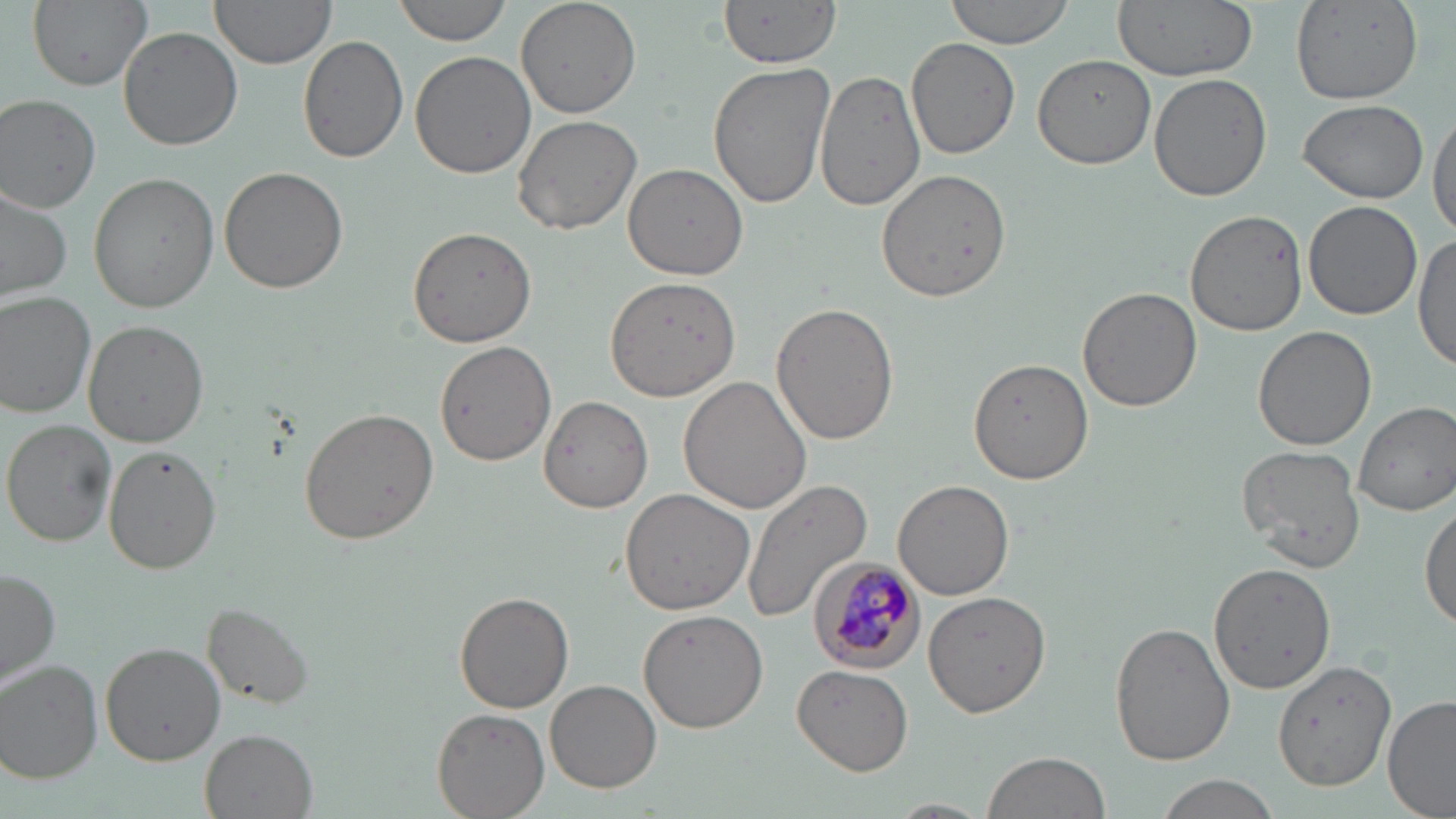

slide_level_diagnosis: Plasmodium malariae
magnification: 1000x
plasmodium_malariae_infected_red_blood_cell_locations: 'approximate bounding boxes as [x1, y1, x2, y2] in pixels: [809, 559, 924, 673]'
preparation: thin blood smear
modality: light microscopy
stain: May-Grünwald-Giemsa
image_size: 1456×819 pixels
uninfected_red_blood_cell_locations: 'approximate bounding boxes as [x1, y1, x2, y2] in pixels: [26, 0, 152, 91], [211, 0, 335, 70], [393, 0, 513, 44], [515, 0, 642, 118], [720, 0, 838, 68], [945, 0, 1079, 49], [1113, 0, 1259, 80], [1289, 1, 1423, 105], [118, 26, 243, 151], [298, 34, 409, 164], [906, 37, 1020, 159], [409, 51, 535, 180], [1032, 54, 1157, 170], [708, 61, 835, 209], [815, 66, 924, 213], [1149, 73, 1272, 204], [1, 95, 101, 212], [1299, 99, 1428, 203], [1429, 107, 1456, 235], [512, 114, 641, 235], [621, 162, 748, 279], [219, 167, 349, 295], [877, 168, 1013, 302], [91, 172, 220, 311], [0, 184, 72, 304], [1303, 201, 1422, 320], [1184, 209, 1308, 334], [406, 225, 539, 349], [1413, 232, 1456, 374], [603, 276, 739, 400], [1077, 287, 1202, 410], [0, 291, 98, 416], [771, 304, 899, 443], [84, 321, 207, 447], [1252, 324, 1377, 449], [435, 341, 558, 467], [970, 358, 1094, 484], [678, 375, 811, 514], [538, 394, 654, 513], [1354, 401, 1456, 515], [299, 408, 439, 544], [3, 419, 116, 545], [1236, 444, 1366, 573], [103, 446, 224, 574], [742, 480, 872, 622], [893, 480, 1015, 602], [618, 487, 754, 615], [1419, 500, 1456, 631], [1206, 563, 1337, 697], [1, 567, 61, 688], [455, 591, 574, 712], [923, 591, 1052, 717], [203, 602, 317, 710], [638, 607, 768, 733], [1110, 621, 1235, 765], [99, 644, 224, 763], [1273, 660, 1396, 790], [1, 661, 103, 782], [792, 664, 913, 775], [545, 680, 662, 793], [1384, 695, 1456, 818], [432, 707, 549, 819], [200, 729, 317, 818], [980, 750, 1112, 819], [1152, 773, 1285, 819], [878, 799, 999, 818]'
field_of_view: one of a larger specimen